Give the extent of all Trypanosoma brucei.
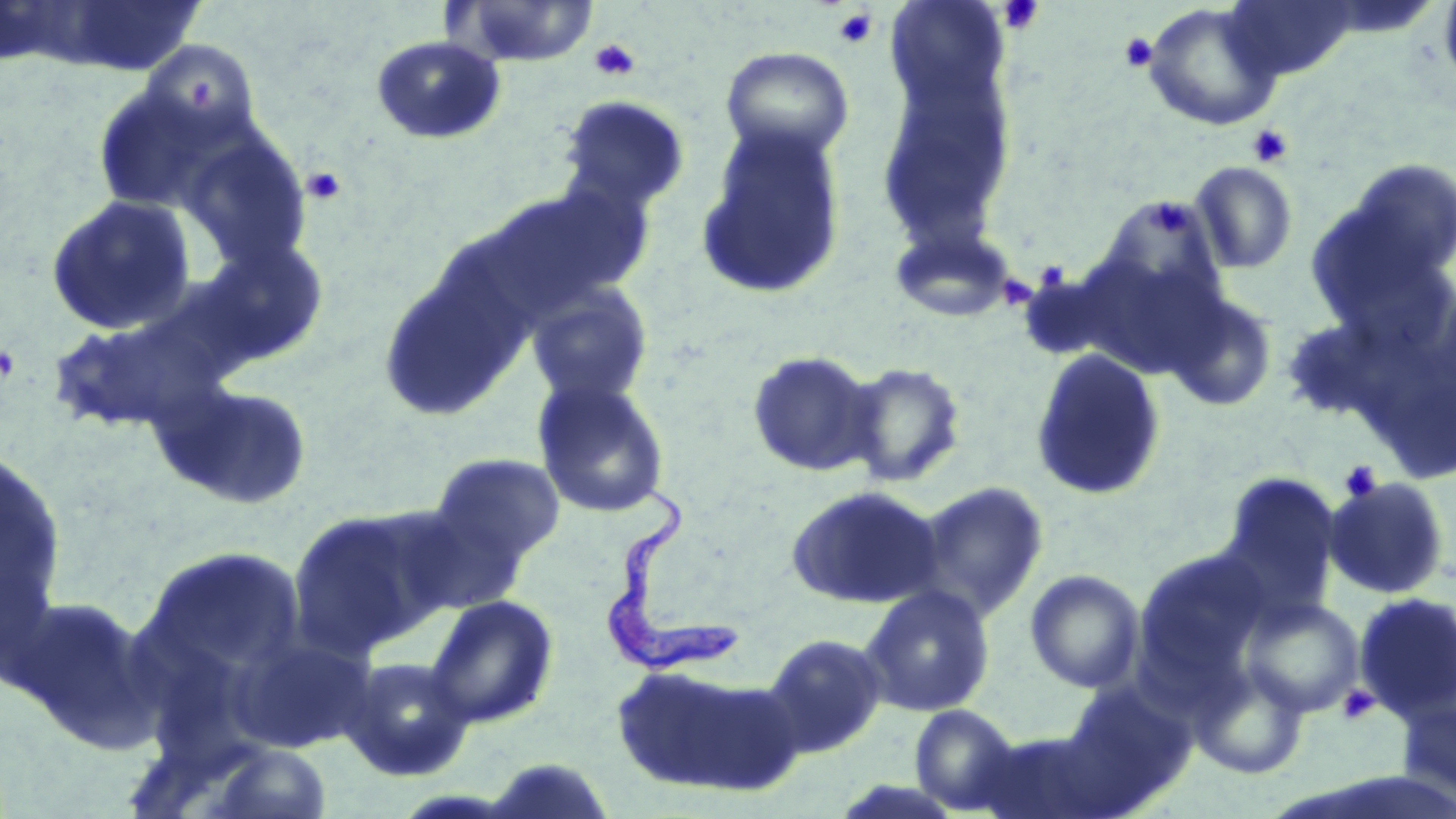
Approximate bounding boxes as named x1/y1/x2/y2 corners in pixels.
Trypanosoma brucei: (x1=611, y1=478, x2=740, y2=678).

Summary:
  - Uninfected red blood cell locations: (x1=454, y1=0, x2=599, y2=68), (x1=885, y1=0, x2=1009, y2=107), (x1=1221, y1=0, x2=1361, y2=81), (x1=1438, y1=0, x2=1456, y2=93), (x1=21, y1=2, x2=210, y2=77), (x1=1143, y1=2, x2=1285, y2=131), (x1=369, y1=35, x2=507, y2=146), (x1=142, y1=40, x2=259, y2=145), (x1=721, y1=46, x2=854, y2=162), (x1=876, y1=70, x2=1019, y2=243), (x1=92, y1=84, x2=225, y2=215), (x1=558, y1=96, x2=690, y2=215), (x1=695, y1=123, x2=848, y2=302), (x1=1341, y1=156, x2=1456, y2=283), (x1=1189, y1=161, x2=1299, y2=274), (x1=475, y1=183, x2=653, y2=323), (x1=44, y1=195, x2=199, y2=336), (x1=1105, y1=196, x2=1227, y2=315), (x1=888, y1=222, x2=1019, y2=323), (x1=196, y1=237, x2=331, y2=370), (x1=377, y1=262, x2=531, y2=422), (x1=526, y1=283, x2=654, y2=407), (x1=1163, y1=290, x2=1279, y2=411), (x1=45, y1=299, x2=244, y2=438), (x1=1279, y1=316, x2=1405, y2=422), (x1=1030, y1=347, x2=1167, y2=502), (x1=745, y1=350, x2=881, y2=478), (x1=842, y1=361, x2=968, y2=488), (x1=531, y1=378, x2=671, y2=518), (x1=153, y1=380, x2=315, y2=512), (x1=0, y1=450, x2=68, y2=654), (x1=428, y1=453, x2=565, y2=569), (x1=1215, y1=471, x2=1343, y2=624), (x1=1323, y1=476, x2=1452, y2=601), (x1=915, y1=481, x2=1049, y2=622), (x1=784, y1=484, x2=945, y2=610), (x1=288, y1=503, x2=461, y2=654), (x1=140, y1=545, x2=309, y2=694), (x1=1134, y1=547, x2=1273, y2=681), (x1=1024, y1=569, x2=1146, y2=693), (x1=858, y1=585, x2=996, y2=717), (x1=1352, y1=591, x2=1456, y2=725), (x1=4, y1=593, x2=162, y2=750), (x1=424, y1=594, x2=560, y2=729), (x1=1241, y1=596, x2=1365, y2=718), (x1=226, y1=629, x2=375, y2=753), (x1=762, y1=632, x2=887, y2=757), (x1=338, y1=656, x2=475, y2=782), (x1=609, y1=661, x2=797, y2=798), (x1=1191, y1=665, x2=1309, y2=780), (x1=1060, y1=678, x2=1199, y2=809), (x1=1397, y1=693, x2=1456, y2=808), (x1=909, y1=704, x2=1024, y2=815), (x1=971, y1=729, x2=1115, y2=818), (x1=214, y1=743, x2=332, y2=818), (x1=479, y1=756, x2=619, y2=819)
  - Platelet locations: (x1=998, y1=1, x2=1044, y2=34), (x1=833, y1=8, x2=878, y2=49), (x1=1119, y1=32, x2=1158, y2=73), (x1=589, y1=39, x2=640, y2=81), (x1=1247, y1=124, x2=1293, y2=168), (x1=301, y1=167, x2=347, y2=206), (x1=1145, y1=198, x2=1192, y2=239), (x1=1037, y1=263, x2=1069, y2=294), (x1=1002, y1=276, x2=1032, y2=305), (x1=1339, y1=460, x2=1383, y2=503), (x1=1336, y1=684, x2=1380, y2=726)
  - Slide-level diagnosis: Trypanosoma brucei
  - Preparation: thin blood smear
  - Magnification: 1000x
  - Modality: optical microscopy
  - Image size: 1456×819 pixels
  - Field of view: single
  - Stain: May-Grünwald-Giemsa